Identify the parasite.
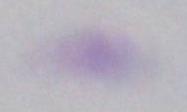
Toxoplasma gondii.

Summary:
  - Magnification: 1000x
  - Modality: micrograph